Report the malaria status of this cell.
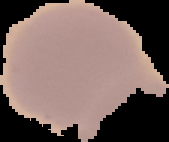
Uninfected.

preparation = thin blood film
image type = segmented cell region on a black background
image size = 169×142 pixels